Describe the morphology of the erythrocytes.
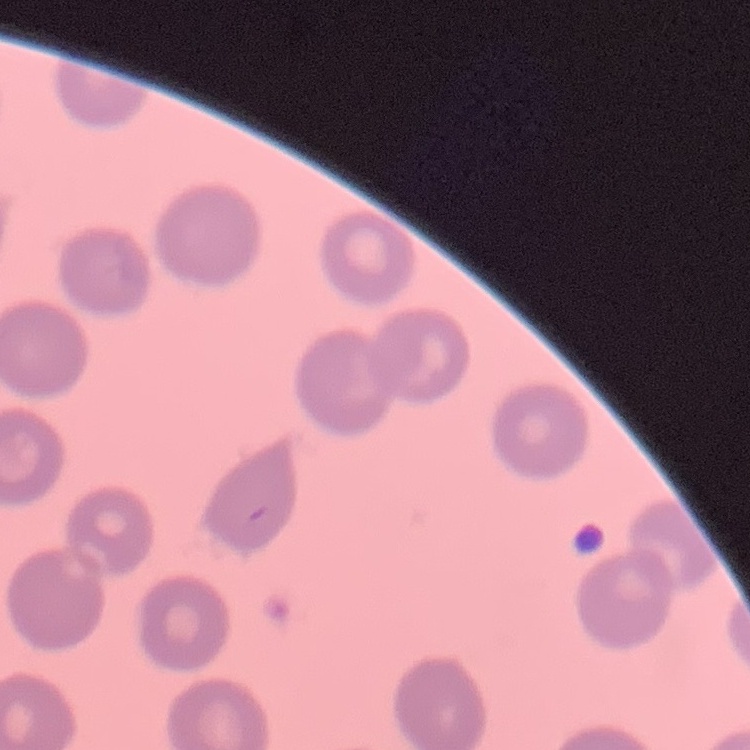

They show no rouleaux formation.

Thin blood smear. Field's or Giemsa stain. Square crop of a larger photomicrograph.